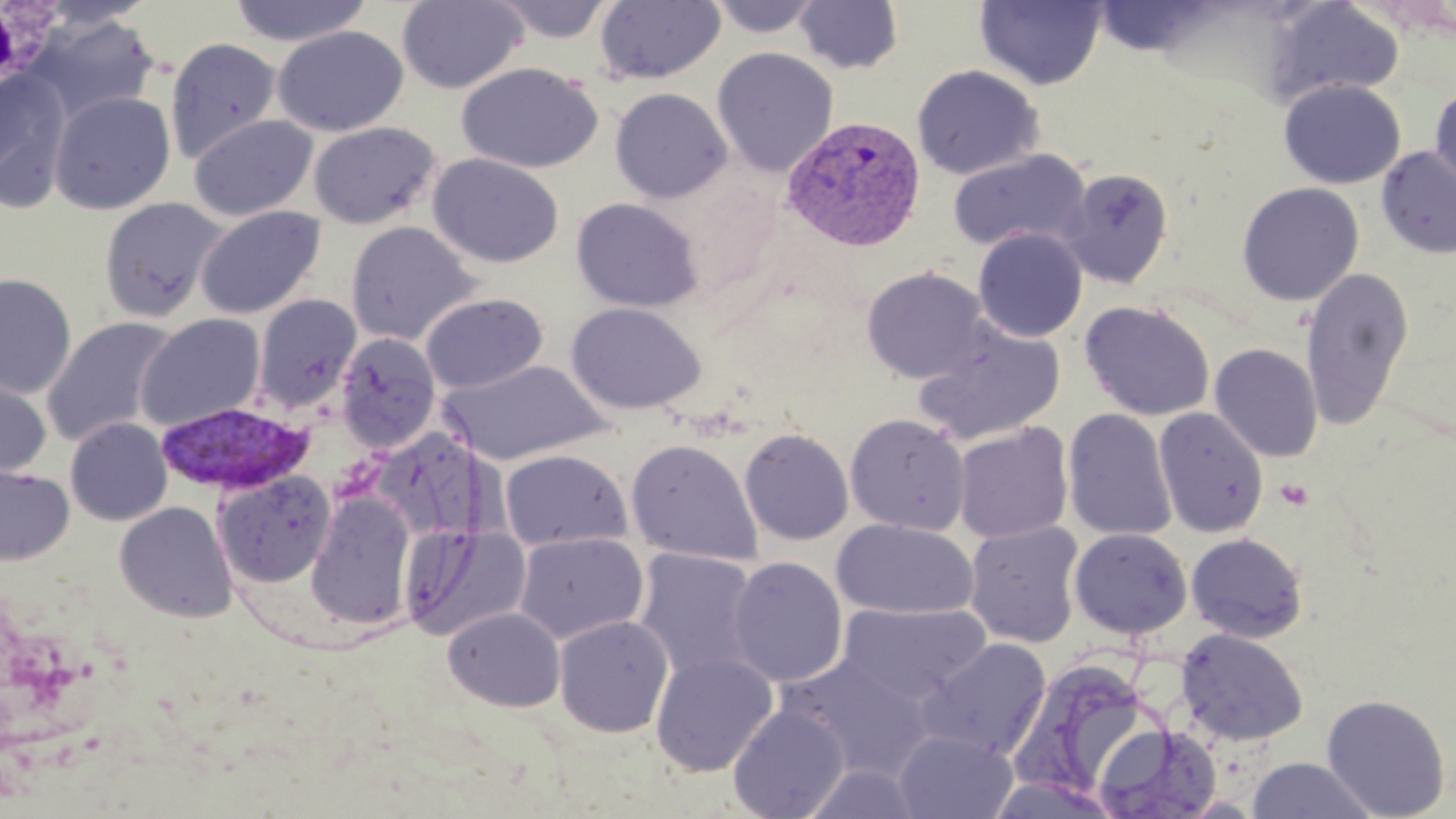

Summary:
  - Coordinate format: approximate bounding boxes as (x1,y1)-(x2,y2) corner pairs in pixels
  - White blood cell locations: (0,0)-(63,88)
  - Uninfected red blood cell locations: (227,0)-(374,47), (397,0)-(527,93), (491,0)-(616,43), (705,0)-(827,38), (975,0)-(1108,91), (594,1)-(726,86), (793,1)-(904,74), (1264,1)-(1404,105), (29,14)-(160,125), (272,25)-(408,137), (165,37)-(283,164), (712,47)-(838,177), (456,61)-(604,173), (911,64)-(1045,179), (0,69)-(72,211), (1278,79)-(1406,190), (1428,84)-(1456,193), (610,87)-(732,204), (49,90)-(175,215), (189,114)-(317,222), (308,121)-(441,230), (1376,146)-(1456,260), (947,150)-(1091,252), (428,153)-(564,269), (1060,167)-(1174,289), (1237,182)-(1364,306), (98,197)-(230,322), (571,198)-(704,313), (195,205)-(325,320), (345,221)-(480,346), (973,228)-(1087,342), (1300,266)-(1414,430), (861,267)-(990,384), (0,273)-(77,398), (420,292)-(548,394), (252,294)-(362,412), (1079,300)-(1215,421), (567,302)-(706,415), (136,313)-(266,430), (41,315)-(179,448), (913,319)-(1065,446), (334,333)-(442,451), (1209,343)-(1323,462), (439,359)-(610,465), (0,372)-(52,480), (1153,406)-(1269,539), (1063,408)-(1178,542), (844,413)-(971,536), (65,417)-(173,525), (953,423)-(1073,544), (739,428)-(854,546), (625,439)-(762,565), (499,449)-(631,551), (0,464)-(74,565), (214,469)-(336,587), (306,492)-(416,628), (114,501)-(238,622), (831,518)-(979,620), (964,522)-(1085,648), (401,524)-(530,642), (1068,528)-(1192,639), (513,532)-(649,645), (1186,533)-(1308,643), (633,547)-(762,684), (728,556)-(848,688), (836,602)-(992,704), (443,606)-(566,712), (553,614)-(674,737), (1176,629)-(1309,746), (916,638)-(1052,760), (650,652)-(778,776), (780,653)-(935,779), (1019,660)-(1152,789), (1321,694)-(1451,819), (728,703)-(850,819), (1093,722)-(1223,818), (894,729)-(1018,818), (1246,756)-(1379,818), (987,776)-(1124,819)
  - Plasmodium vivax-infected red blood cell locations: (781,115)-(926,252), (154,401)-(313,496)
  - Slide-level diagnosis: Plasmodium vivax
  - Modality: optical microscopy
  - Preparation: thin blood film
  - Magnification: 1000x
  - Stain: May-Grünwald-Giemsa
  - Field of view: single
  - Image size: 1456×819 pixels